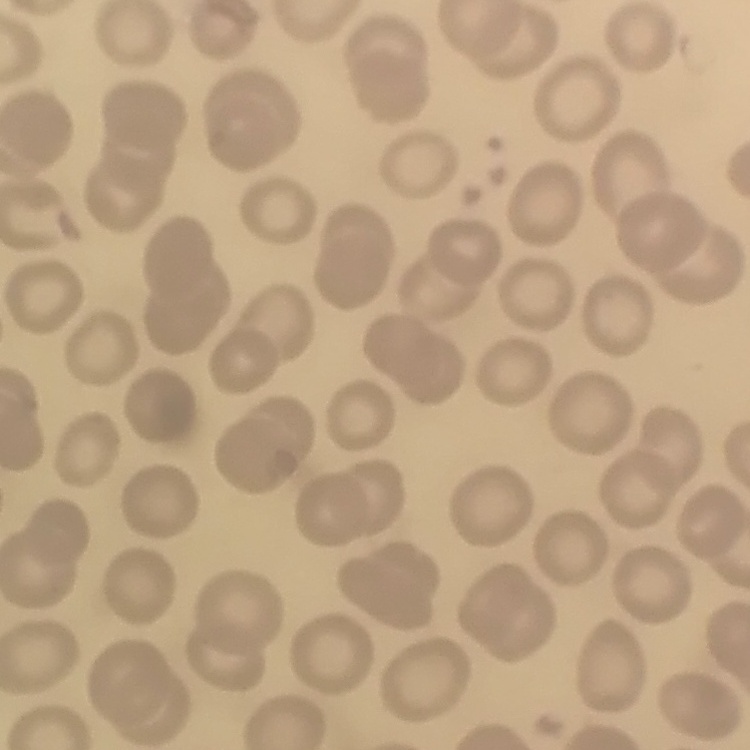

red blood cell morphology = no rouleaux formation
stain = Field's or Giemsa
preparation = thin blood film
image type = square crop of a larger photomicrograph